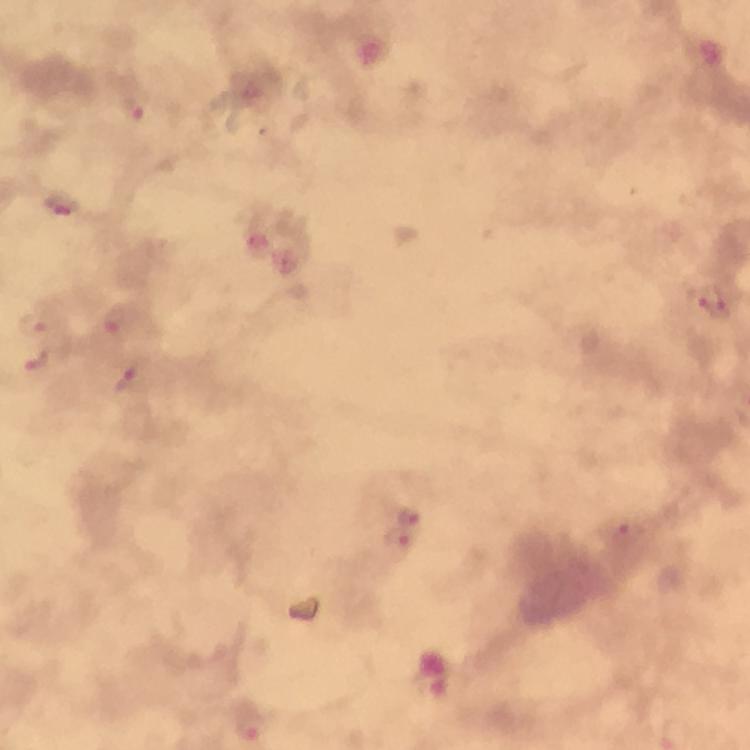

Approximate object centers, in pixels from the top-left corner.
Summary:
  - Plasmodium parasite locations: (x=133, y=109), (x=63, y=199), (x=716, y=303), (x=116, y=322), (x=37, y=323), (x=38, y=361), (x=127, y=380), (x=409, y=516), (x=625, y=535), (x=400, y=538), (x=249, y=728)
  - Capture: smartphone photograph through a microscope
  - Image size: 750×750 pixels
  - Context: from a malaria diagnostic workup
  - Immersion oil: used
  - Cropped from: a single field of view
  - Magnification: 100x
  - Preparation: thick smear
  - Stain: Giemsa